Comment on the morphology of the red blood cells.
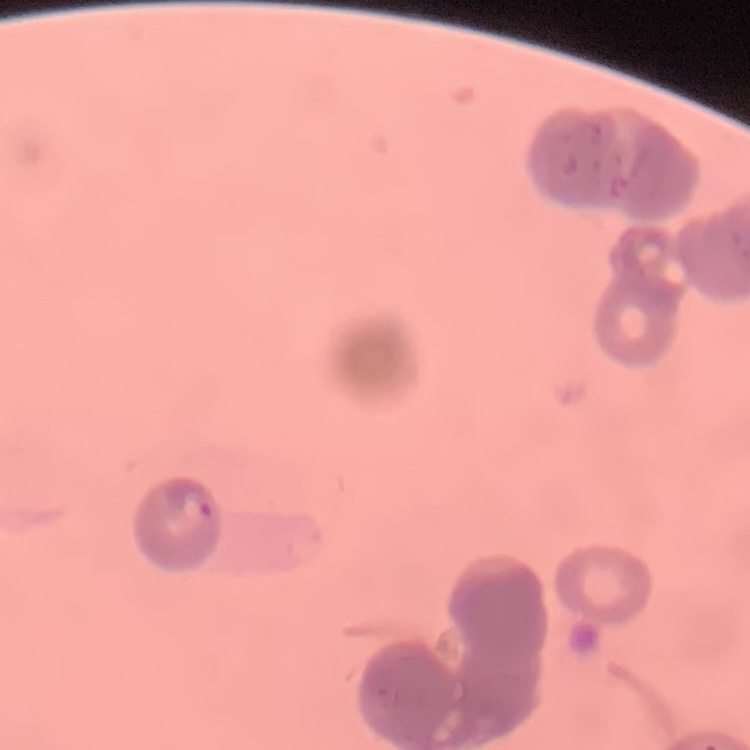

Rouleaux formation.

Thin peripheral smear. Field's or Giemsa stain. Square crop of a larger photomicrograph.